State which parasite is depicted.
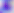

Toxoplasma gondii.

Summary:
  - Modality: photomicrograph
  - Magnification: 400x